Comment on the morphology of the erythrocytes.
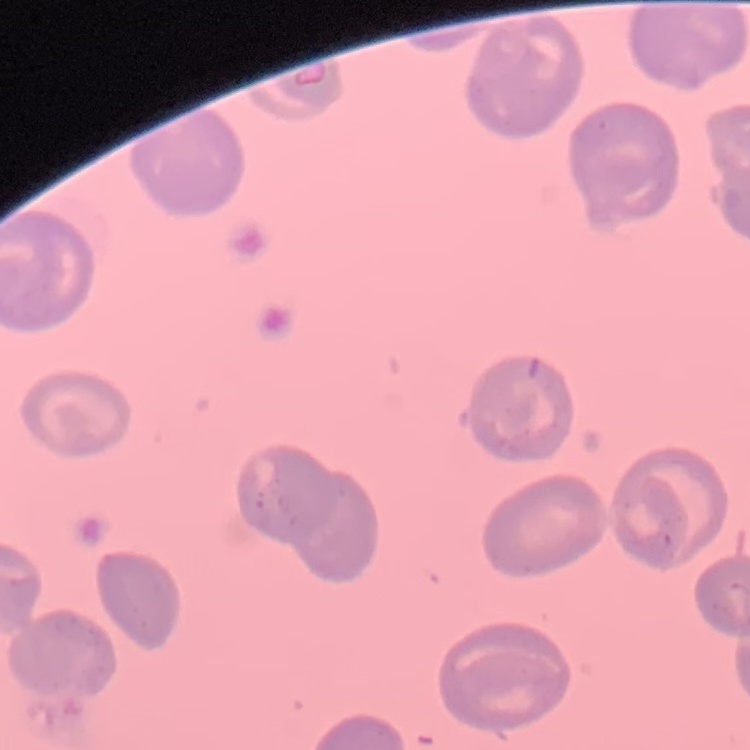
They show no rouleaux formation.

Summary:
  - Preparation: thin blood smear
  - Image type: square crop of a larger photomicrograph
  - Stain: Field's or Giemsa